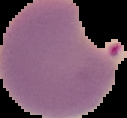

Image is 127×118 pixels. Cell region segmented out of the field of view; the surrounding area is masked to black. From a thin blood film. Result: Plasmodium parasites detected.